Identify the parasite.
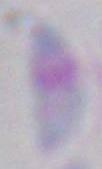
This is Toxoplasma gondii.

Summary:
  - Magnification: 1000x
  - Modality: photomicrograph